Comment on the morphology of the erythrocytes.
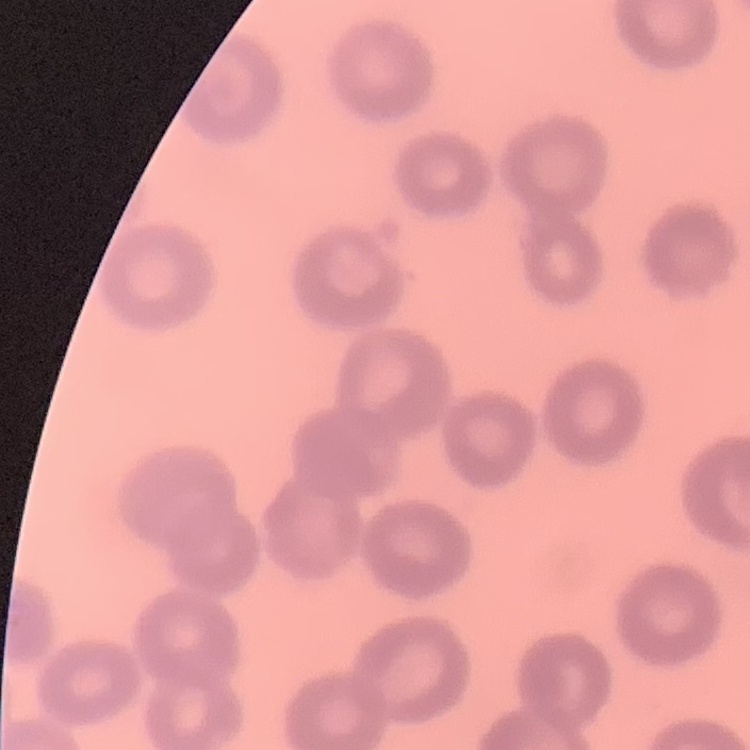
No rouleaux formation.

Square crop of a larger photomicrograph. Thin peripheral smear. Field's or Giemsa stain.